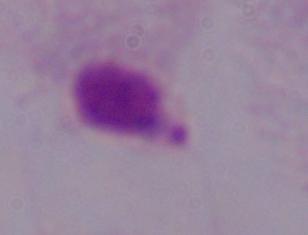

{
  "modality": "photomicrograph",
  "magnification": "1000x",
  "identification": "trichomonad"
}